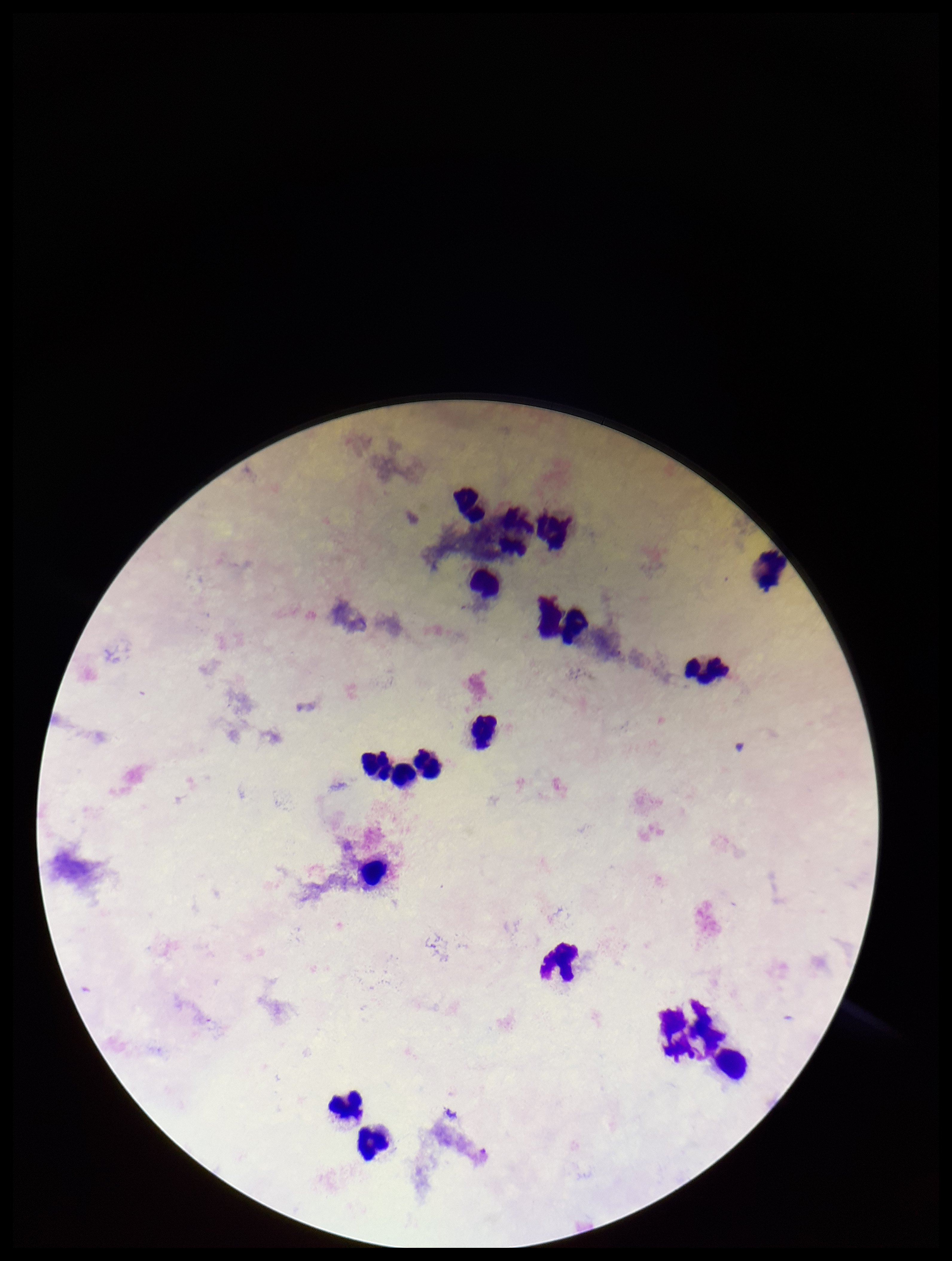 Parasite count: 0. Plasmodium parasites: none detected. Preparation: thick. Leukocyte count: 18. Patient malaria status: negative. Smartphone photograph taken through the eyepiece of a microscope. Single field of view. Image is 952×1261 pixels. Stained with Giemsa.